Give the extent of all uninfected red blood cells.
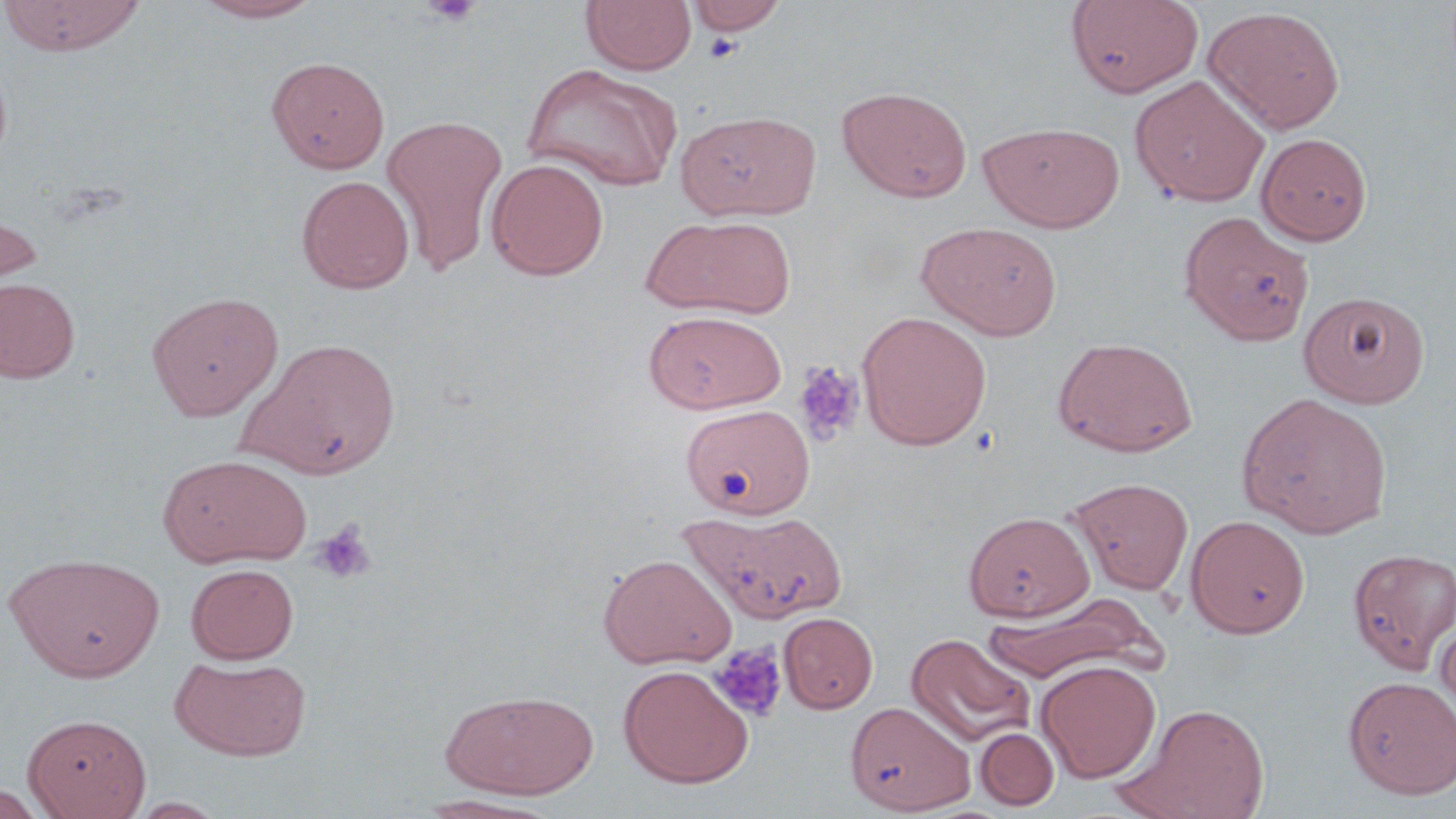
Approximate bounding boxes as named x1/y1/x2/y2 corners in pixels.
Uninfected red blood cells: (x1=0, y1=0, x2=148, y2=55), (x1=189, y1=0, x2=327, y2=23), (x1=581, y1=0, x2=697, y2=75), (x1=1065, y1=0, x2=1204, y2=99), (x1=688, y1=1, x2=786, y2=35), (x1=1202, y1=5, x2=1346, y2=134), (x1=266, y1=56, x2=390, y2=173), (x1=520, y1=63, x2=681, y2=192), (x1=1130, y1=75, x2=1270, y2=208), (x1=837, y1=86, x2=972, y2=202), (x1=676, y1=111, x2=821, y2=221), (x1=381, y1=114, x2=508, y2=275), (x1=979, y1=122, x2=1125, y2=233), (x1=1255, y1=132, x2=1372, y2=245), (x1=486, y1=158, x2=609, y2=280), (x1=297, y1=175, x2=415, y2=294), (x1=0, y1=203, x2=43, y2=312), (x1=1178, y1=211, x2=1315, y2=346), (x1=687, y1=218, x2=795, y2=317), (x1=640, y1=219, x2=750, y2=314), (x1=916, y1=222, x2=1063, y2=341), (x1=0, y1=277, x2=80, y2=383), (x1=1299, y1=291, x2=1430, y2=408), (x1=147, y1=292, x2=283, y2=421), (x1=644, y1=310, x2=786, y2=414), (x1=856, y1=311, x2=993, y2=451), (x1=1053, y1=336, x2=1197, y2=457), (x1=244, y1=338, x2=400, y2=480), (x1=1237, y1=392, x2=1393, y2=538), (x1=681, y1=403, x2=814, y2=519), (x1=158, y1=453, x2=311, y2=568), (x1=1068, y1=477, x2=1194, y2=595), (x1=681, y1=507, x2=847, y2=624), (x1=963, y1=511, x2=1094, y2=621), (x1=1185, y1=514, x2=1310, y2=638), (x1=1348, y1=549, x2=1456, y2=673), (x1=5, y1=552, x2=166, y2=682), (x1=599, y1=553, x2=736, y2=669), (x1=185, y1=563, x2=299, y2=664), (x1=981, y1=596, x2=1156, y2=684), (x1=1434, y1=611, x2=1456, y2=723), (x1=778, y1=612, x2=878, y2=713), (x1=907, y1=633, x2=1035, y2=748), (x1=170, y1=655, x2=312, y2=761), (x1=1035, y1=660, x2=1162, y2=783), (x1=618, y1=665, x2=754, y2=788), (x1=1343, y1=675, x2=1456, y2=800), (x1=440, y1=689, x2=600, y2=800), (x1=847, y1=701, x2=974, y2=814), (x1=1117, y1=702, x2=1272, y2=819), (x1=23, y1=713, x2=151, y2=818), (x1=975, y1=728, x2=1059, y2=810), (x1=0, y1=784, x2=48, y2=819), (x1=411, y1=795, x2=560, y2=818), (x1=124, y1=797, x2=232, y2=818).

Platelet locations: (x1=419, y1=1, x2=484, y2=26), (x1=701, y1=32, x2=744, y2=64), (x1=794, y1=362, x2=865, y2=446), (x1=310, y1=521, x2=376, y2=585), (x1=709, y1=643, x2=787, y2=722). Slide-level diagnosis: negative for blood parasites. Image is 1456×819 pixels. May-Grünwald-Giemsa stain. Light microscopy. Single field of view. 1000x magnification. Thin blood smear.